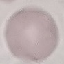
Result: no malaria parasites seen. Automatically extracted cell patch, resized to 64 × 64 pixels. Thin smear of blood. Acquired by smartphone through the microscope eyepiece. Giemsa stain.